State which parasite is depicted.
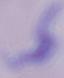
A trypanosome.

Micrograph. 1000x magnification.